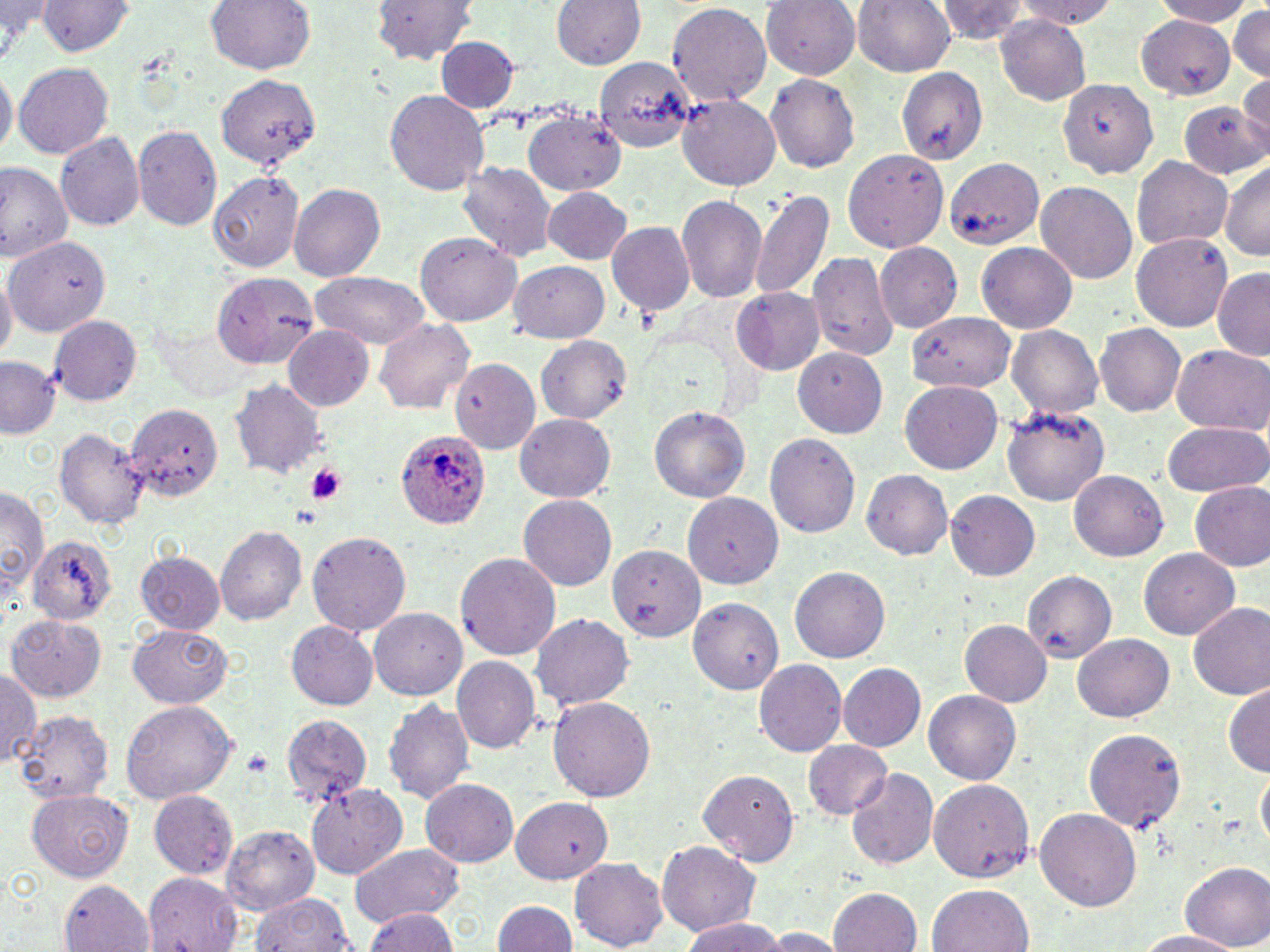

Summary:
  - Coordinate format: approximate bounding boxes as (x1, y1, x2, y2) in pixels
  - Plasmodium ovale-infected red blood cell locations: (394, 430, 493, 529)
  - Uninfected red blood cell locations: (206, 0, 316, 75), (371, 0, 478, 63), (551, 0, 646, 70), (851, 0, 956, 76), (934, 0, 1029, 46), (1016, 0, 1115, 30), (1152, 0, 1254, 25), (760, 1, 861, 80), (0, 2, 55, 61), (34, 2, 136, 57), (666, 2, 772, 107), (1229, 5, 1269, 82), (1137, 14, 1237, 98), (995, 17, 1089, 104), (437, 36, 518, 112), (596, 57, 697, 152), (13, 61, 114, 158), (0, 63, 16, 161), (896, 67, 987, 165), (1236, 72, 1269, 156), (216, 74, 320, 169), (765, 74, 861, 173), (1057, 79, 1159, 179), (385, 88, 491, 196), (676, 93, 780, 191), (1177, 98, 1269, 179), (520, 108, 628, 197), (132, 125, 222, 231), (55, 131, 146, 231), (840, 147, 948, 252), (1133, 155, 1234, 252), (943, 156, 1044, 250), (0, 160, 72, 261), (458, 161, 557, 263), (1219, 162, 1270, 260), (208, 172, 306, 272), (1036, 181, 1136, 283), (288, 183, 386, 281), (748, 186, 836, 304), (542, 187, 631, 264), (675, 194, 767, 303), (605, 219, 695, 315), (1130, 230, 1233, 332), (414, 232, 518, 326), (5, 237, 108, 336), (976, 241, 1076, 332), (874, 242, 964, 333), (807, 250, 898, 361), (509, 261, 609, 342), (1213, 267, 1270, 359), (0, 268, 16, 360), (311, 270, 430, 348), (212, 272, 317, 367), (731, 287, 825, 374), (48, 314, 142, 406), (905, 314, 1015, 393), (374, 319, 475, 412), (1095, 323, 1185, 417), (1006, 324, 1103, 420), (282, 325, 374, 410), (536, 335, 632, 422), (1170, 343, 1269, 434), (791, 346, 888, 438), (1, 357, 60, 439), (450, 358, 539, 452), (230, 379, 327, 478), (900, 380, 1004, 473), (125, 402, 220, 504), (648, 404, 750, 503), (1001, 406, 1111, 505), (515, 413, 615, 501), (1161, 421, 1269, 499), (53, 426, 150, 529), (765, 433, 860, 537), (861, 469, 952, 559), (1067, 470, 1169, 562), (1190, 480, 1270, 571), (0, 484, 50, 605), (946, 490, 1040, 580), (684, 493, 784, 589), (518, 494, 616, 590), (214, 525, 307, 626), (305, 530, 412, 634), (28, 536, 118, 626), (609, 544, 704, 643), (1138, 548, 1240, 639), (135, 550, 225, 634), (455, 551, 560, 660), (789, 565, 889, 662), (1022, 570, 1116, 660), (691, 597, 784, 694), (1187, 601, 1270, 699), (369, 608, 466, 700), (7, 613, 106, 701), (530, 614, 633, 710), (959, 620, 1052, 707), (285, 621, 379, 710), (128, 623, 232, 707), (1073, 634, 1173, 720), (451, 656, 541, 754), (754, 659, 847, 755), (837, 663, 926, 751), (0, 664, 40, 769), (1224, 680, 1270, 776), (924, 690, 1021, 784), (548, 696, 655, 802), (382, 697, 475, 804), (120, 699, 237, 804), (13, 711, 115, 805), (279, 713, 374, 804), (1083, 726, 1187, 835), (802, 739, 892, 818), (1256, 762, 1270, 854), (698, 769, 801, 864), (849, 770, 940, 871), (419, 779, 519, 867), (926, 779, 1035, 882), (305, 782, 409, 879), (27, 788, 133, 881), (146, 790, 238, 879), (511, 797, 613, 883), (1034, 807, 1142, 913), (223, 825, 320, 915), (656, 840, 760, 937), (345, 842, 465, 927), (570, 859, 668, 950), (1181, 864, 1269, 949), (141, 872, 245, 952), (56, 880, 154, 950), (929, 884, 1034, 952), (829, 887, 922, 952), (252, 893, 358, 951), (491, 899, 577, 952), (360, 907, 459, 951), (680, 918, 790, 951), (760, 927, 849, 950), (1133, 930, 1242, 952)
  - Platelet locations: (305, 465, 346, 504), (243, 753, 273, 777)
  - Slide-level diagnosis: Plasmodium ovale
  - Field of view: one of a larger specimen
  - Stain: May-Grünwald-Giemsa
  - Image size: 1270×952 pixels
  - Magnification: 1000x
  - Modality: optical microscopy
  - Preparation: thin blood smear